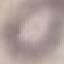

Summary:
  - Result: negative for malaria parasites
  - Preparation: thin blood film
  - Image type: cell patch, automatically extracted from a larger field of view and resized to 64 × 64 pixels
  - Stain: Giemsa
  - Capture: smartphone through the microscope eyepiece